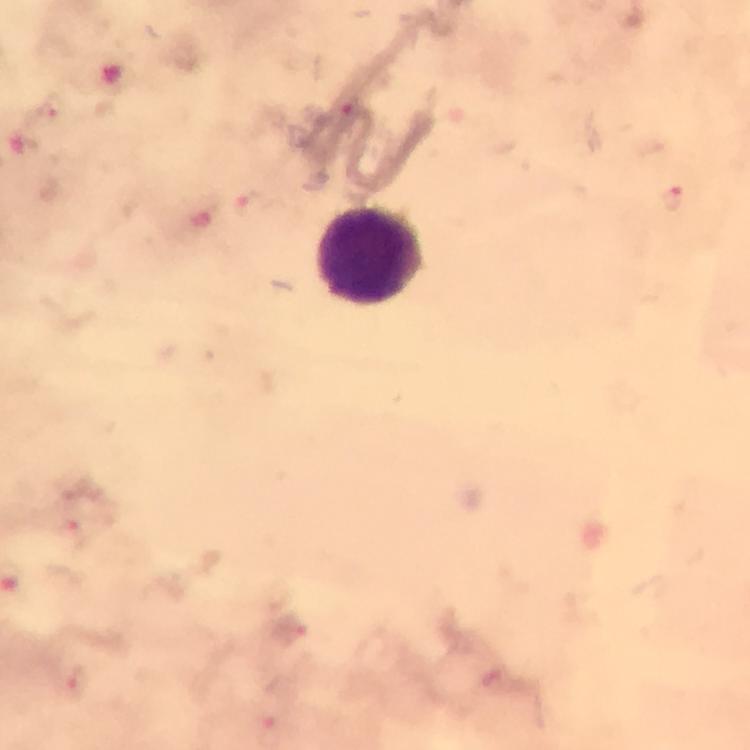

image size = 750×750 pixels
capture = smartphone mounted on the microscope
preparation = thick smear
stain = Giemsa
immersion oil = used
cropped from = one field of view
context = from a diagnostic examination for malaria
Plasmodium parasite locations = approximate centers as [x, y] in pixels: [348, 104], [50, 107], [673, 197], [247, 205], [70, 528], [292, 632]
leukocyte locations = approximate centers as [x, y] in pixels: [371, 257]
magnification = 100x